Report the malaria status.
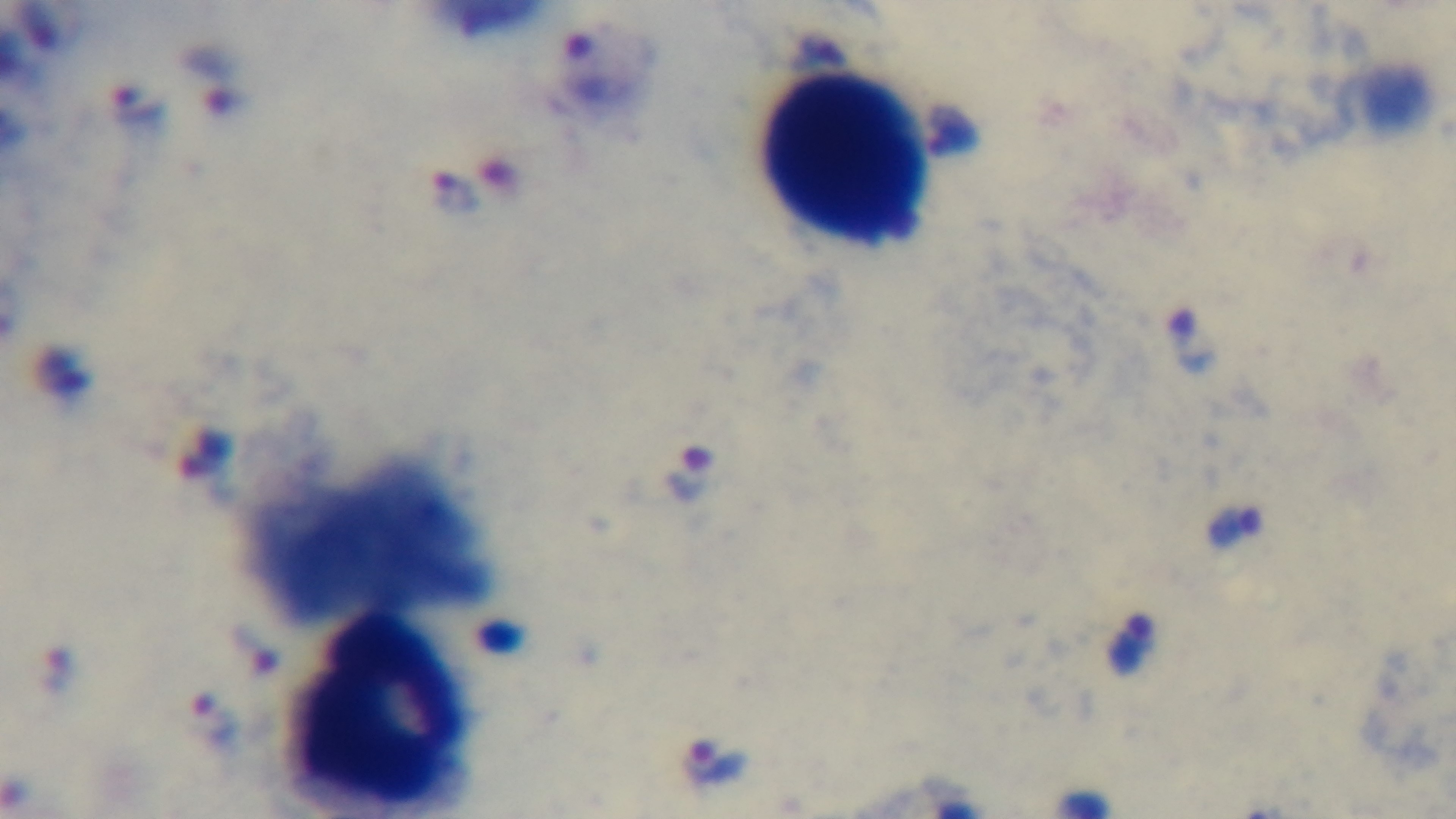

It is infected.

Summary:
  - Preparation: thick smear
  - Field of view: single
  - Stain: Giemsa
  - Modality: light microscopy
  - Objective: 100x oil immersion
  - Capture: mounted 4K digital camera